Locate every uninfected red blood cell.
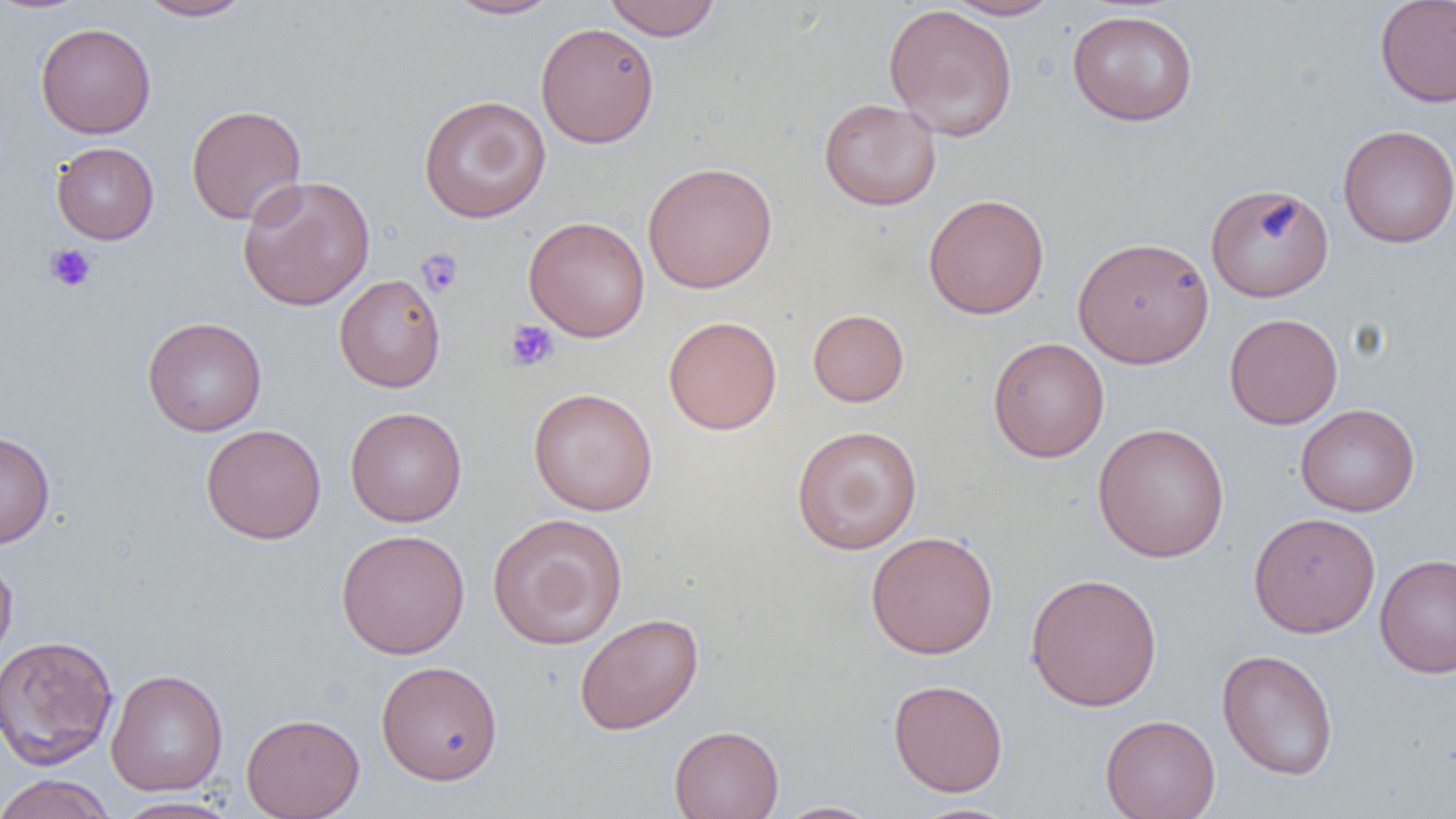

Approximate bounding boxes as [x1, y1, x2, y2] in pixels.
Uninfected red blood cells: [134, 0, 254, 21], [443, 0, 562, 20], [603, 0, 721, 40], [942, 0, 1064, 20], [1374, 0, 1456, 108], [882, 3, 1019, 142], [1066, 9, 1199, 126], [535, 22, 659, 148], [36, 23, 155, 139], [418, 94, 551, 223], [818, 98, 942, 211], [186, 104, 307, 225], [1338, 124, 1456, 248], [51, 142, 159, 244], [642, 160, 778, 294], [237, 174, 375, 311], [1205, 182, 1334, 302], [923, 193, 1049, 319], [523, 216, 650, 342], [1072, 236, 1213, 369], [334, 274, 446, 393], [808, 309, 909, 407], [1224, 313, 1343, 429], [142, 316, 267, 436], [663, 316, 782, 435], [987, 337, 1109, 462], [528, 387, 658, 515], [1295, 403, 1420, 516], [345, 406, 467, 527], [1092, 422, 1230, 563], [201, 424, 326, 544], [791, 424, 923, 555], [0, 429, 55, 549], [1248, 511, 1381, 637], [487, 512, 628, 650], [336, 528, 470, 659], [865, 530, 998, 659], [0, 553, 18, 672], [1375, 553, 1456, 679], [1025, 572, 1163, 711], [574, 612, 704, 735], [0, 634, 119, 770], [1216, 648, 1339, 781], [376, 660, 503, 785], [106, 668, 228, 796], [888, 679, 1008, 797], [241, 712, 365, 819], [1100, 714, 1220, 819], [669, 725, 784, 819], [0, 773, 116, 819], [109, 796, 242, 818], [771, 800, 884, 818], [906, 802, 1024, 819].

slide-level diagnosis = negative for blood parasites
modality = light microscopy
field of view = single
preparation = thin blood smear
image size = 1456×819 pixels
magnification = 1000x
platelet locations = approximate bounding boxes as [x1, y1, x2, y2] in pixels: [44, 243, 98, 292], [417, 248, 463, 297], [504, 320, 558, 372]